Classify this cell by malaria status.
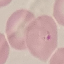

Parasitized.

Summary:
  - Stain: Giemsa
  - Capture: smartphone through the microscope eyepiece
  - Image type: cell patch, automatically extracted from a larger field of view and resized to 64 × 64 pixels
  - Preparation: thin blood smear